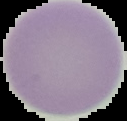

Summary:
  - Malaria status: uninfected
  - Image type: segmented cell region with the area outside set to black
  - Image size: 127×121 pixels
  - Preparation: thin blood smear